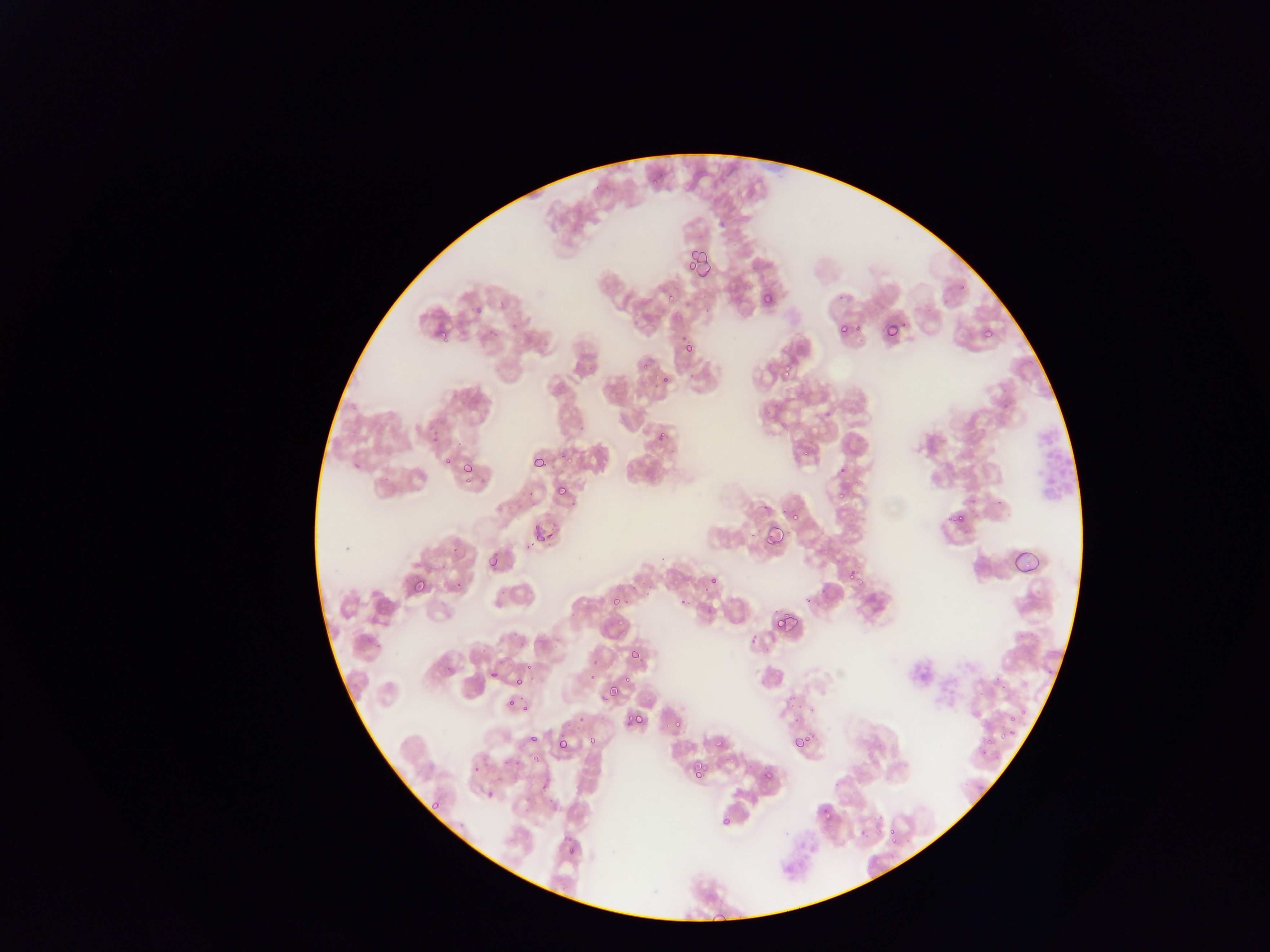

malaria parasite locations = approximate bounding boxes as left top right bottom in pixels: 651 175 659 183; 686 240 710 271; 686 260 697 270; 692 263 711 281; 959 282 970 292; 666 293 681 308; 761 293 773 305; 883 322 902 339; 837 324 851 337; 436 328 448 340; 983 329 993 338; 684 343 695 355; 638 359 655 374; 780 361 795 376; 660 375 669 384; 797 388 808 399; 777 414 796 434; 657 430 667 442; 802 440 817 456; 442 456 453 467; 533 456 546 467; 352 462 360 470; 462 462 473 473; 839 484 851 497; 556 485 568 496; 786 508 799 520; 949 510 966 524; 529 521 554 548; 764 523 784 545; 819 540 836 559; 1013 542 1043 576; 451 545 460 554; 488 554 499 567; 846 568 861 585; 409 576 427 594; 709 576 718 584; 453 580 462 590; 609 597 619 607; 774 607 796 630; 613 619 626 633; 628 649 640 660; 523 662 539 674; 490 669 499 679; 615 673 629 693; 514 677 524 687; 609 682 621 696; 784 693 800 706; 506 697 516 707; 1016 701 1027 721; 522 703 531 712; 792 710 803 723; 632 712 646 724; 578 715 587 724; 999 718 1018 742; 672 719 683 731; 791 734 807 748; 528 735 539 745; 555 737 570 750; 587 738 597 746; 714 738 726 749; 974 748 990 758; 508 757 520 768; 692 762 705 776; 472 764 481 775; 763 770 774 780; 477 780 503 808; 432 800 441 810; 820 805 833 817; 721 815 731 827; 887 825 897 835; 886 836 904 851; 567 846 576 855; 705 907 733 930
country = Ghana
capture = mobile-phone photograph through a microscope
image size = 1270×952 pixels
field of view = single
preparation = thin blood film
leukocyte locations = approximate bounding boxes as left top right bottom in pixels: 1033 415 1077 507